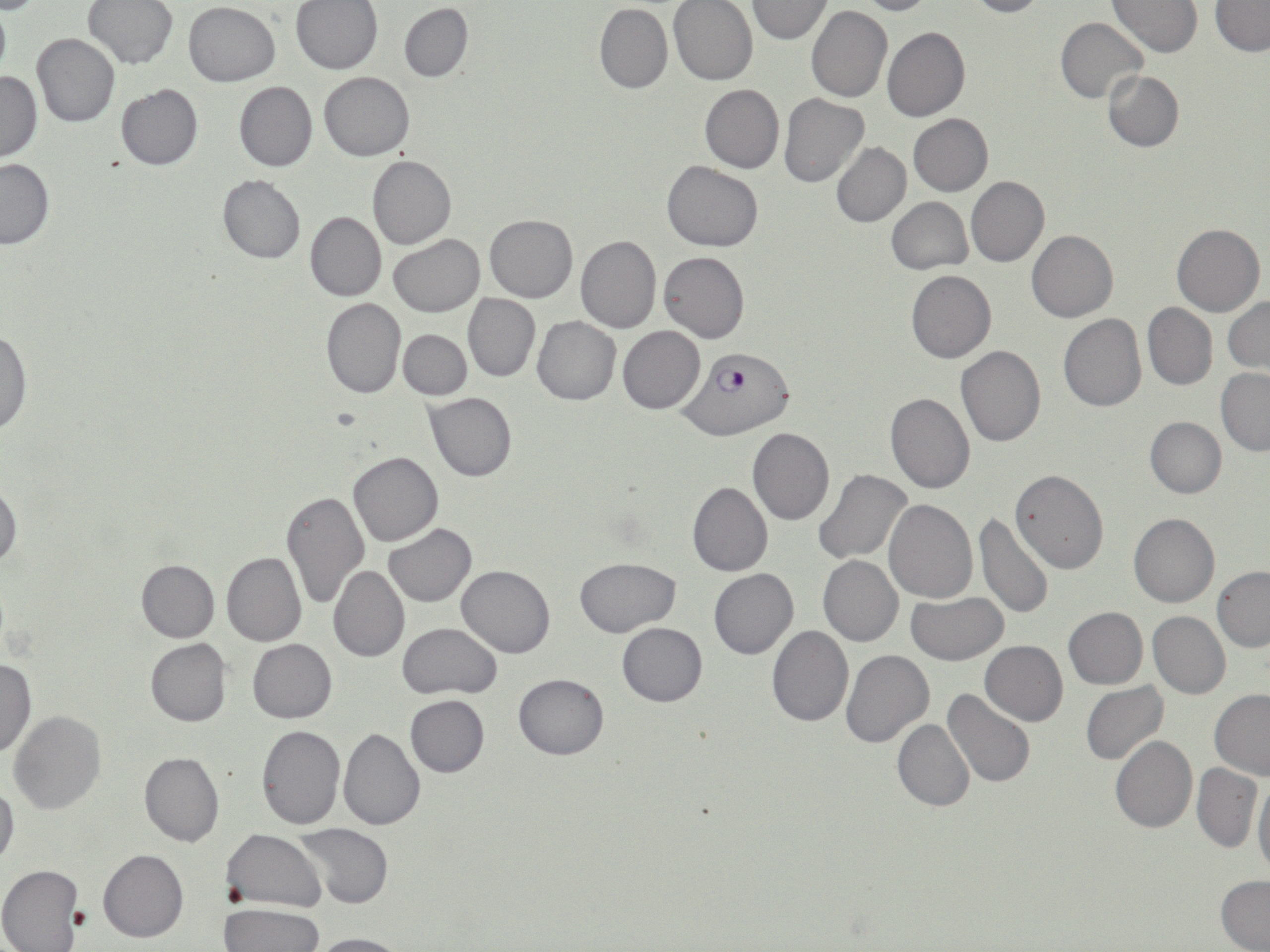

Summary:
  - Coordinate format: approximate bounding boxes as [x1, y1, x2, y2] in pixels
  - Plasmodium falciparum-infected red blood cell locations: [680, 349, 795, 439]
  - Uninfected red blood cell locations: [851, 0, 937, 15], [962, 0, 1050, 18], [84, 1, 177, 70], [291, 1, 384, 74], [669, 1, 759, 85], [745, 1, 833, 42], [1109, 1, 1203, 56], [1211, 1, 1270, 55], [184, 2, 280, 85], [399, 3, 473, 82], [594, 4, 672, 93], [806, 4, 892, 103], [1054, 18, 1148, 104], [883, 26, 970, 122], [32, 33, 120, 127], [0, 70, 42, 161], [1102, 70, 1184, 151], [319, 71, 414, 160], [234, 80, 317, 171], [115, 84, 203, 170], [700, 84, 783, 173], [779, 93, 868, 187], [909, 114, 993, 196], [831, 142, 910, 227], [368, 155, 456, 249], [0, 158, 53, 248], [663, 161, 763, 252], [217, 176, 305, 263], [966, 176, 1049, 266], [887, 196, 972, 274], [305, 212, 385, 302], [486, 214, 577, 303], [1172, 222, 1264, 316], [1026, 230, 1118, 322], [389, 233, 485, 317], [575, 235, 661, 333], [659, 251, 749, 343], [907, 270, 996, 362], [464, 294, 540, 381], [321, 297, 405, 398], [1224, 298, 1270, 372], [1143, 303, 1217, 390], [1058, 313, 1146, 412], [531, 315, 620, 404], [619, 326, 705, 414], [0, 327, 32, 438], [399, 329, 471, 399], [955, 344, 1046, 448], [1216, 369, 1270, 455], [886, 391, 974, 493], [425, 392, 517, 481], [1145, 417, 1226, 498], [749, 428, 834, 525], [348, 451, 444, 546], [814, 469, 913, 564], [1010, 469, 1109, 573], [0, 479, 21, 571], [688, 480, 773, 576], [281, 491, 368, 608], [884, 499, 977, 603], [1128, 513, 1219, 608], [974, 514, 1052, 621], [383, 524, 478, 606], [222, 552, 306, 646], [819, 554, 903, 646], [574, 557, 681, 636], [136, 559, 219, 641], [329, 565, 409, 662], [456, 565, 554, 657], [1212, 566, 1270, 652], [708, 569, 798, 659], [905, 592, 1008, 664], [1064, 607, 1147, 689], [1148, 610, 1229, 699], [397, 622, 502, 699], [617, 623, 708, 706], [766, 624, 854, 728], [145, 638, 231, 726], [247, 639, 335, 723], [980, 640, 1067, 725], [840, 650, 933, 749], [0, 657, 35, 758], [514, 673, 608, 759], [1080, 682, 1168, 766], [943, 688, 1036, 788], [1210, 691, 1270, 780], [406, 695, 490, 776], [8, 712, 106, 816], [892, 719, 973, 812], [256, 723, 346, 831], [337, 728, 425, 830], [1110, 736, 1197, 832], [139, 752, 223, 847], [1191, 763, 1261, 852], [1253, 779, 1270, 881], [0, 780, 19, 870], [291, 823, 393, 908], [222, 829, 326, 911], [98, 848, 188, 942], [0, 865, 85, 951], [1216, 876, 1270, 951], [220, 902, 324, 952], [306, 932, 409, 952]
  - Slide-level diagnosis: Plasmodium falciparum
  - Magnification: 1000x
  - Field of view: single
  - Modality: optical microscopy
  - Image size: 1270×952 pixels
  - Stain: May-Grünwald-Giemsa
  - Preparation: thin blood smear